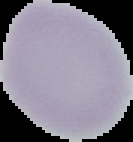
image type = segmented cell region with the area outside set to black
image size = 133×142 pixels
preparation = thin blood film
result = no malaria parasites detected